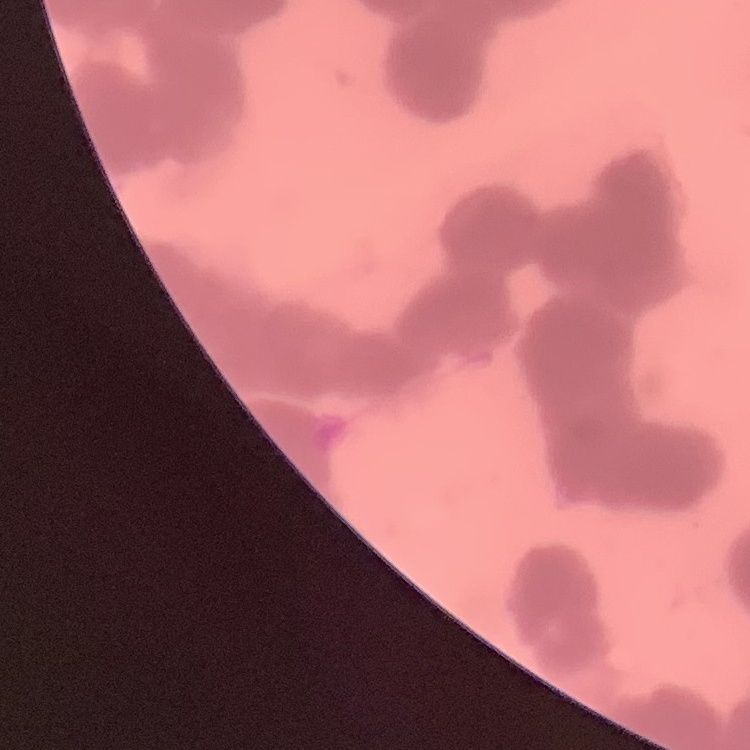
erythrocyte morphology = rouleaux formation
image type = square crop of a larger photomicrograph
stain = Field's or Giemsa
preparation = thin peripheral smear